Report the malaria status of this cell.
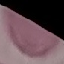

It is uninfected.

Thin blood film. Cell patch, automatically extracted from a larger field of view and resized to 64 × 64 pixels. Acquired by smartphone through the microscope eyepiece. Giemsa-stained preparation.